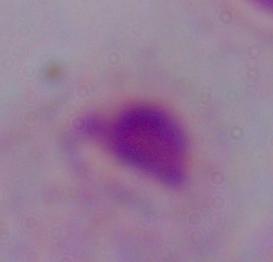
Captured at 1000x magnification. A trichomonad is seen. Photomicrograph.